Identify the blood parasite species.
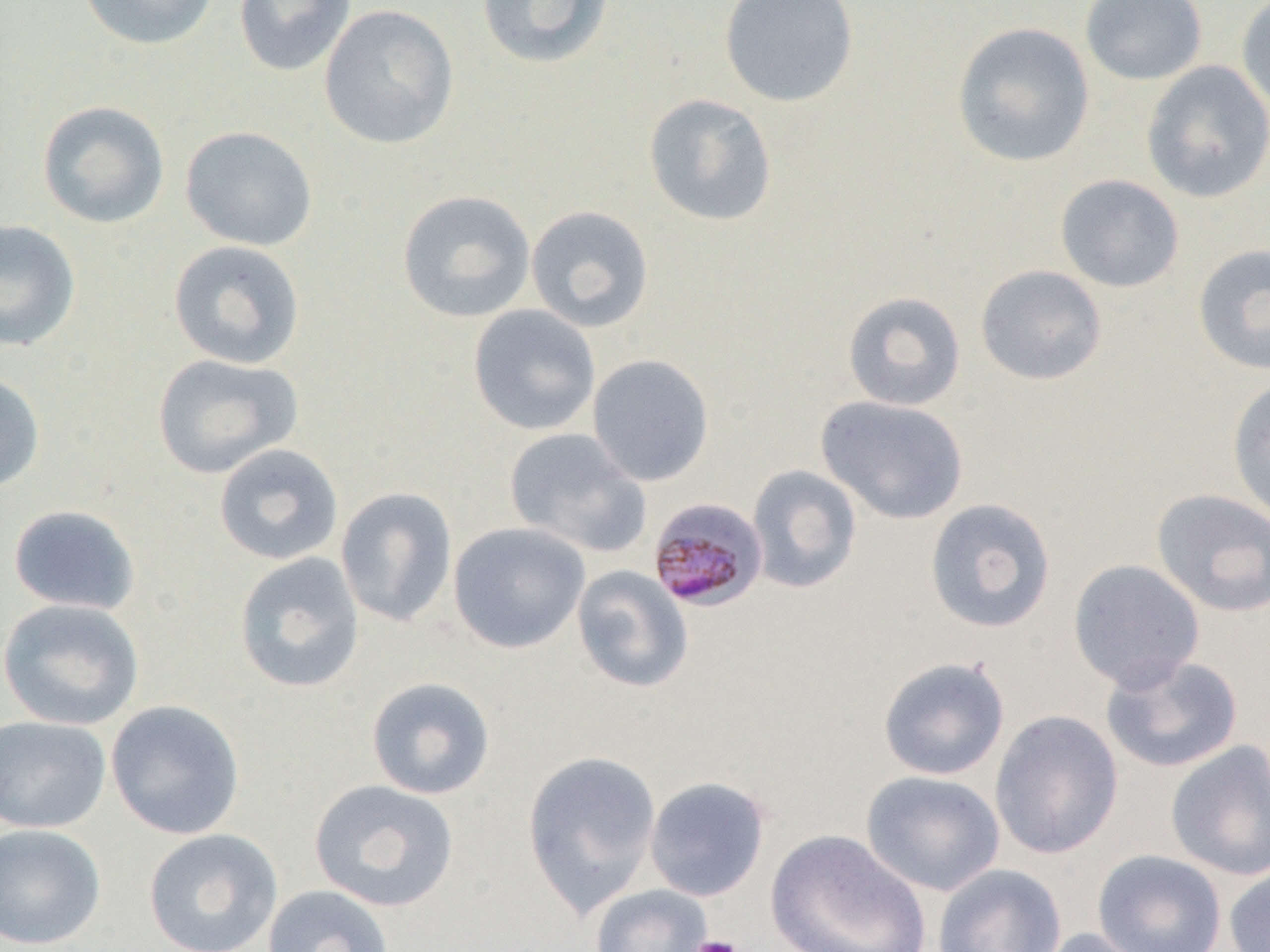
Plasmodium malariae.

Approximate bounding boxes as [x1, y1, x2, y2] in pixels. Uninfected red blood cell locations: [78, 0, 219, 51], [233, 0, 356, 77], [476, 0, 615, 70], [718, 0, 859, 108], [1078, 0, 1208, 86], [1235, 0, 1270, 116], [319, 4, 459, 149], [952, 21, 1095, 168], [1140, 61, 1270, 203], [642, 93, 778, 227], [36, 100, 170, 229], [180, 125, 318, 251], [1055, 174, 1185, 293], [397, 189, 536, 323], [525, 205, 655, 333], [0, 219, 81, 352], [168, 240, 306, 370], [1191, 243, 1270, 376], [975, 264, 1108, 386], [842, 291, 966, 411], [468, 304, 601, 436], [151, 353, 303, 479], [587, 353, 714, 486], [0, 371, 46, 494], [1226, 376, 1270, 524], [815, 395, 969, 525], [504, 427, 651, 559], [213, 442, 344, 565], [747, 464, 862, 594], [335, 486, 457, 628], [1151, 489, 1270, 617], [924, 498, 1056, 634], [7, 504, 140, 615], [448, 521, 591, 654], [233, 551, 365, 694], [1068, 558, 1205, 692], [571, 565, 694, 693], [0, 598, 145, 730], [1100, 654, 1243, 773], [877, 656, 1010, 781], [365, 676, 496, 800], [105, 699, 246, 840], [990, 709, 1123, 859], [0, 715, 111, 833], [1165, 740, 1270, 881], [522, 749, 662, 916], [861, 770, 1005, 896], [644, 776, 770, 902], [308, 779, 460, 913], [0, 822, 106, 949], [143, 828, 283, 952], [765, 829, 931, 952], [1092, 849, 1227, 952], [932, 863, 1067, 952], [1223, 863, 1270, 952], [262, 884, 394, 952], [588, 884, 712, 952], [1031, 927, 1157, 952]. Plasmodium malariae-infected red blood cell locations: [647, 497, 769, 612]. Platelet locations: [690, 935, 743, 952]. Image is 1270×952 pixels. 1000x magnification. Single field of view. Thin blood smear. Optical microscopy.